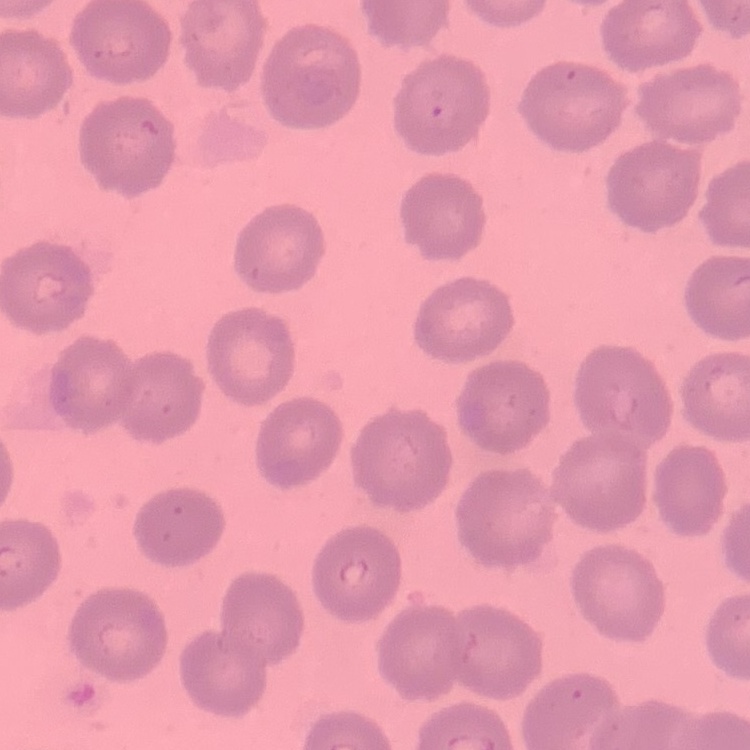

erythrocyte morphology = no rouleaux formation
stain = Field's or Giemsa
preparation = thin blood film
image type = square crop of a larger photomicrograph